Assess this cell for malaria.
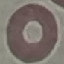
It is uninfected.

Giemsa stain. Automatically extracted cell patch, resized to 64 × 64 pixels. Thin smear of blood. Acquired by smartphone through the microscope eyepiece.